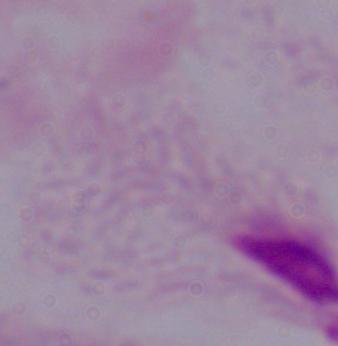
Summary:
  - Magnification: 1000x
  - Modality: micrograph
  - Identification: trichomonad